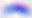
400x magnification. Toxoplasma gondii is seen. Photomicrograph.